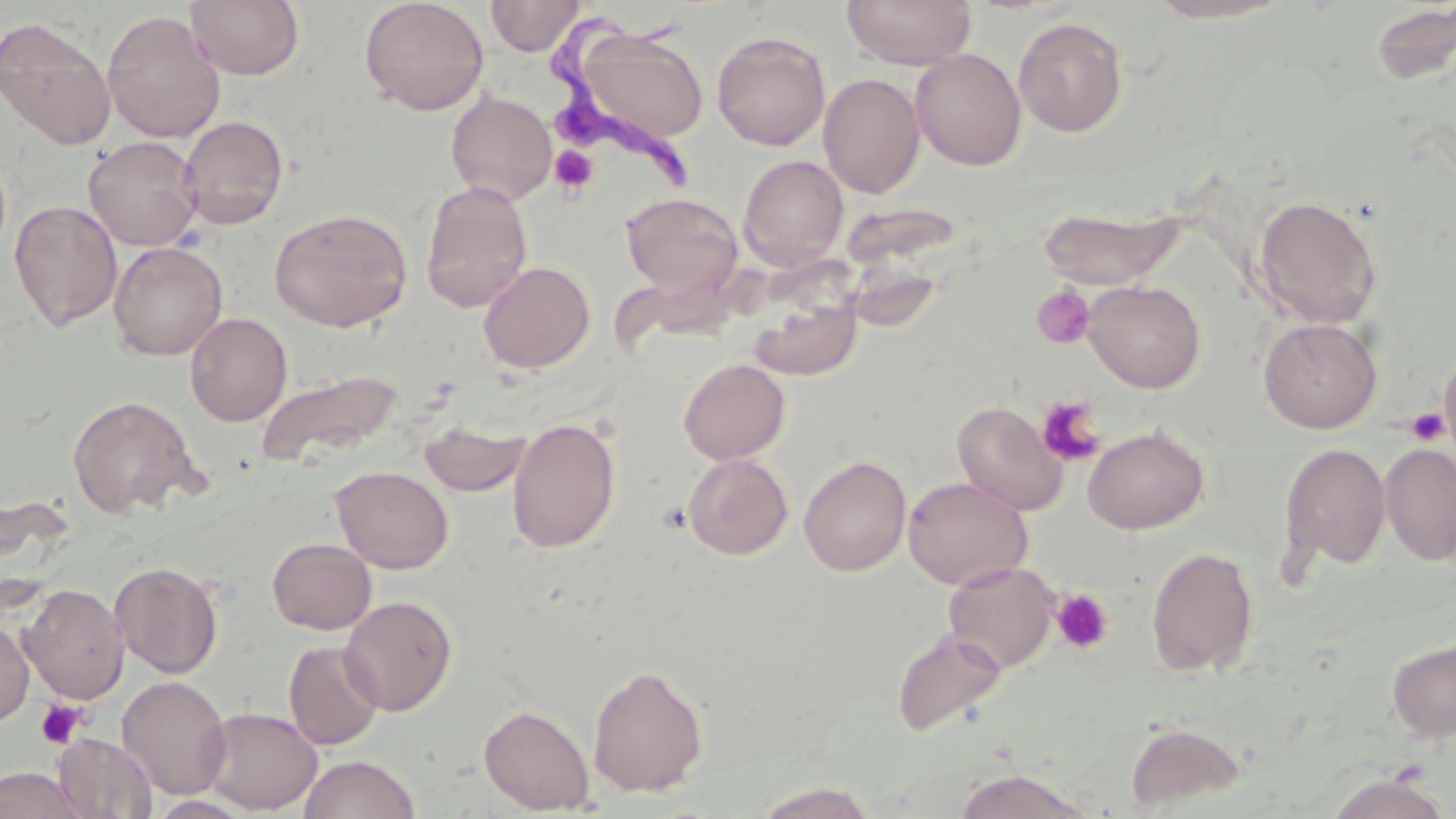
Approximate bounding boxes as (x1, y1, x2, y2) in pixels. Uninfected red blood cell locations: (185, 0, 304, 80), (359, 0, 490, 115), (486, 0, 583, 56), (841, 0, 977, 70), (1140, 0, 1294, 24), (1368, 3, 1456, 86), (101, 10, 225, 144), (1013, 16, 1128, 137), (0, 17, 117, 151), (576, 28, 709, 146), (712, 31, 830, 151), (910, 49, 1026, 170), (818, 73, 925, 198), (445, 90, 557, 206), (178, 115, 289, 230), (83, 135, 203, 251), (738, 155, 848, 270), (420, 181, 533, 313), (621, 193, 743, 301), (1252, 195, 1383, 329), (9, 199, 122, 331), (1035, 205, 1187, 290), (269, 208, 413, 332), (108, 241, 228, 361), (478, 261, 595, 374), (1082, 279, 1206, 393), (748, 292, 863, 382), (185, 312, 292, 426), (1258, 318, 1383, 433), (1438, 346, 1456, 468), (678, 358, 791, 464), (255, 370, 402, 468), (67, 395, 202, 518), (951, 400, 1068, 516), (506, 416, 621, 554), (419, 419, 531, 497), (1082, 425, 1210, 534), (1278, 442, 1391, 574), (1379, 443, 1456, 565), (682, 452, 793, 560), (798, 455, 912, 577), (331, 466, 453, 573), (903, 476, 1032, 590), (267, 538, 376, 634), (1145, 546, 1260, 679), (110, 561, 224, 679), (942, 561, 1059, 673), (19, 584, 129, 703), (338, 595, 458, 716), (0, 619, 34, 727), (891, 628, 1007, 738), (1387, 638, 1456, 742), (282, 640, 385, 750), (587, 665, 708, 797), (116, 675, 232, 800), (479, 705, 595, 815), (198, 706, 323, 815), (1125, 721, 1247, 813), (53, 733, 157, 819), (298, 754, 420, 819), (0, 766, 89, 819), (948, 768, 1096, 818), (1323, 772, 1452, 818), (752, 781, 879, 819). Platelet locations: (550, 146, 598, 195), (1031, 286, 1095, 350), (1036, 396, 1106, 467), (1407, 406, 1450, 447), (1051, 588, 1114, 654), (36, 699, 86, 748). Trypanosoma brucei locations: (527, 5, 701, 204). Slide-level diagnosis: Trypanosoma brucei. May-Grünwald-Giemsa-stained preparation. Thin blood film. Image is 1456×819 pixels. Optical microscopy. Captured at 1000x magnification. One field of a larger specimen.